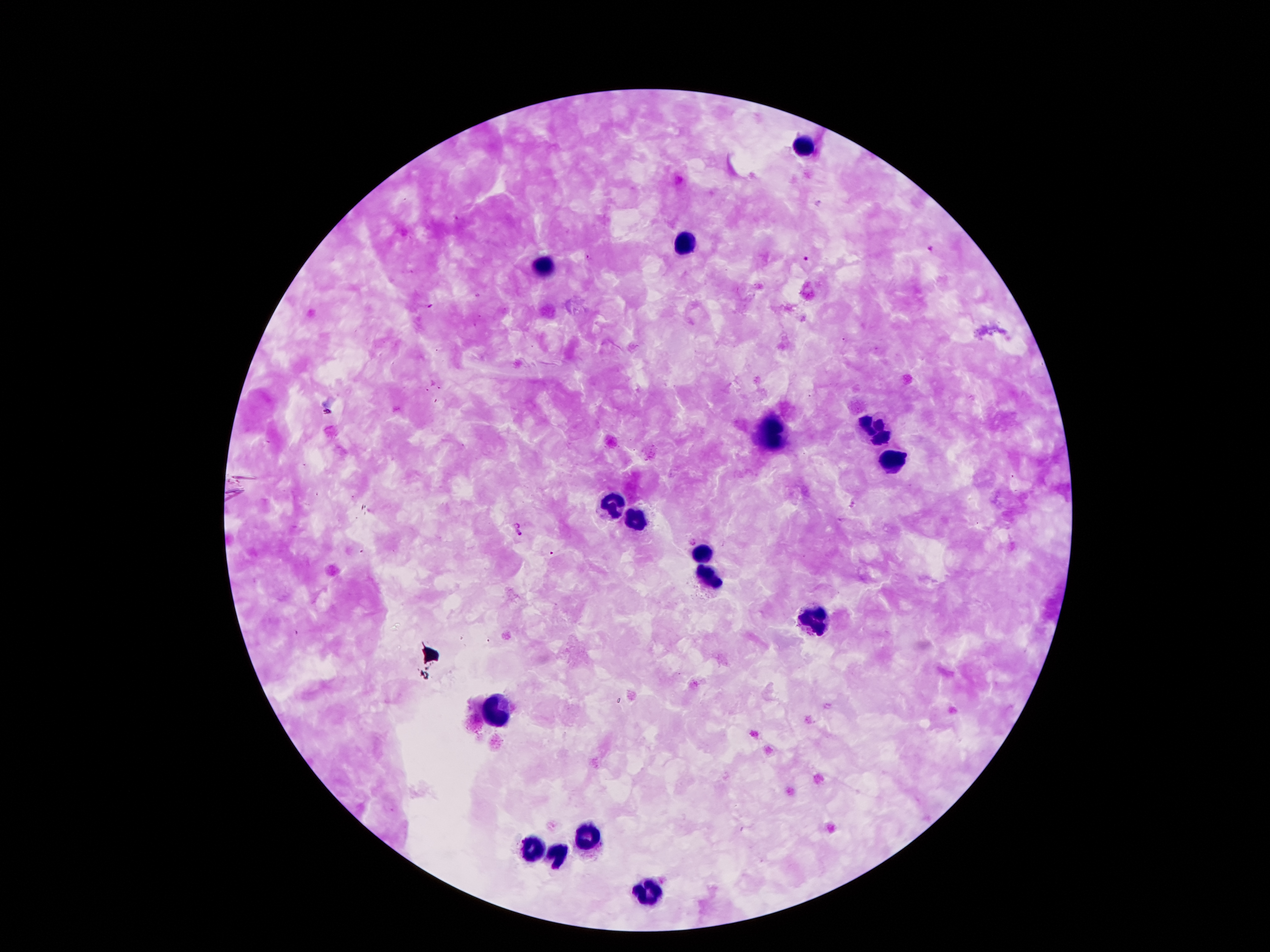
Approximate centers as {x, y} in pixels.
Summary:
  - Plasmodium parasite locations: {456, 218}, {930, 248}, {590, 257}, {806, 259}, {479, 294}, {431, 306}, {1014, 477}, {515, 522}, {519, 535}
  - Leukocyte locations: {799, 147}, {684, 246}, {545, 271}, {877, 432}, {768, 434}, {892, 462}, {615, 508}, {636, 518}, {701, 554}, {709, 575}, {816, 621}, {497, 710}, {586, 836}, {531, 847}, {560, 854}, {644, 892}
  - Patient malaria status: infected with Plasmodium falciparum
  - Magnification: 100x
  - Preparation: thick peripheral-blood smear
  - Capture: smartphone through the microscope eyepiece
  - Image size: 1270×952 pixels
  - Field of view: single
  - Stain: Giemsa